Classify this cell by malaria status.
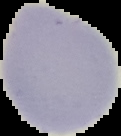
It is uninfected.

From a thin blood film. Image is 121×136 pixels. Segmented cell region on a black background.